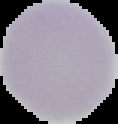
From a thin blood film. The area outside the segmented cell region is set to black. Image is 118×124 pixels. Malaria status: uninfected.